Locate every blood parasite and identify its species.
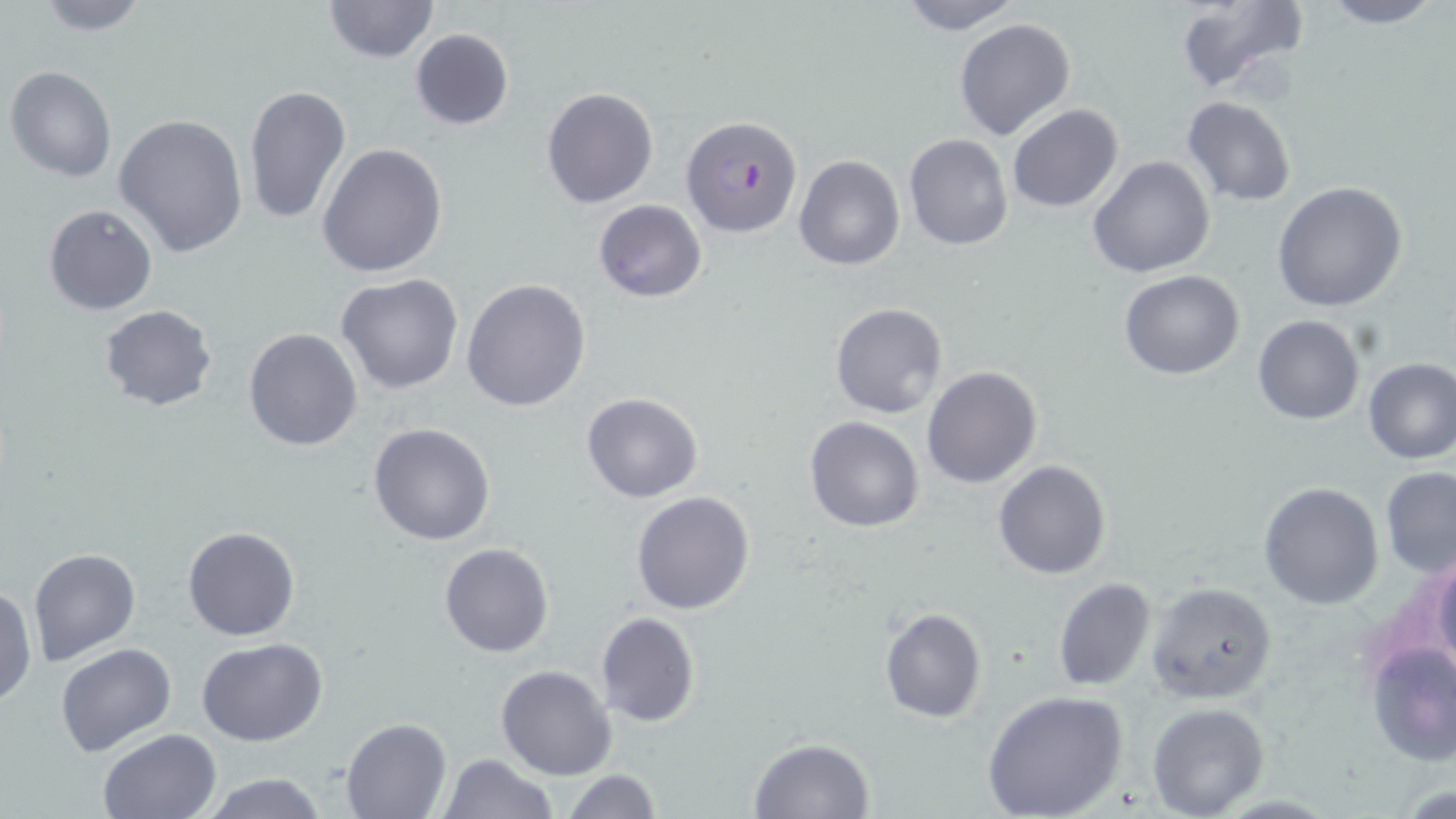
Approximate bounding boxes as (x1,y1)-(x2,y2) corner pairs in pixels.
Plasmodium falciparum-infected red blood cells: (681,114)-(804,240).
No Plasmodium ovale, Plasmodium malariae, Plasmodium vivax, Babesia divergens, or Trypanosoma brucei observed.

Summary:
  - Uninfected red blood cell locations: (28,0)-(155,36), (323,0)-(437,63), (896,0)-(1023,34), (1173,0)-(1311,101), (1312,0)-(1445,28), (953,17)-(1076,140), (408,29)-(513,131), (5,65)-(118,183), (242,84)-(351,226), (540,87)-(660,209), (1181,95)-(1297,207), (1007,104)-(1124,215), (115,114)-(248,258), (902,134)-(1014,252), (316,143)-(448,278), (1088,154)-(1215,278), (793,156)-(905,270), (1271,182)-(1408,314), (593,199)-(706,304), (43,203)-(158,316), (1119,270)-(1244,379), (335,273)-(464,395), (462,278)-(591,412), (830,303)-(947,420), (99,304)-(219,411), (1251,315)-(1364,424), (243,327)-(362,450), (1362,358)-(1456,464), (920,365)-(1043,489), (581,392)-(703,504), (803,414)-(925,532), (367,422)-(496,546), (992,460)-(1111,580), (1379,467)-(1456,577), (1259,482)-(1384,609), (629,490)-(755,616), (182,526)-(301,641), (438,542)-(554,658), (1424,545)-(1456,672), (27,546)-(141,666), (1052,577)-(1157,691), (1146,580)-(1277,703), (1,584)-(36,710), (878,607)-(986,725), (595,612)-(700,727), (197,637)-(328,746), (1364,639)-(1456,767), (54,642)-(177,758), (496,665)-(616,780), (981,689)-(1130,819), (1147,703)-(1269,817), (340,717)-(451,819), (97,728)-(221,818), (748,738)-(875,819), (440,753)-(558,818), (560,769)-(663,819), (198,773)-(332,818)
  - Slide-level diagnosis: Plasmodium falciparum
  - Magnification: 1000x
  - Modality: light microscopy
  - Image size: 1456×819 pixels
  - Stain: May-Grünwald-Giemsa
  - Preparation: thin blood smear
  - Field of view: one of a larger specimen